Assess this cell for malaria.
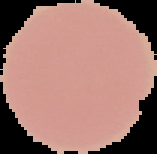

Uninfected.

image_type: segmented cell region with the area outside set to black
preparation: thin blood film
image_size: 157×154 pixels